Locate and identify every blood parasite.
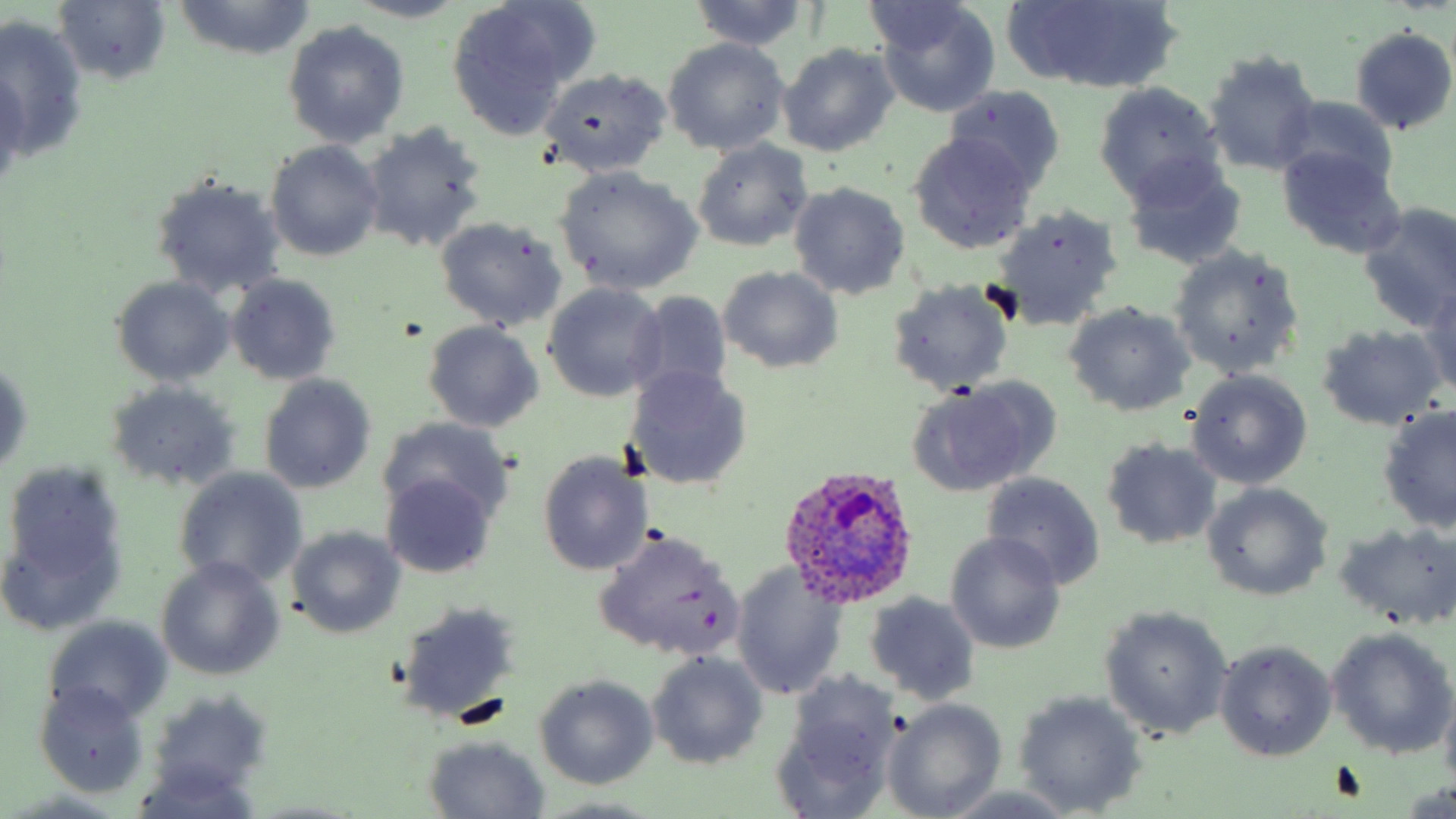
Approximate bounding boxes as named x1/y1/x2/y2 corners in pixels.
Plasmodium ovale-infected red blood cells: (x1=779, y1=466, x2=920, y2=608).
No Plasmodium falciparum, Plasmodium malariae, Plasmodium vivax, Babesia divergens, or Trypanosoma brucei observed.

Summary:
  - Uninfected red blood cell locations: (x1=54, y1=0, x2=173, y2=88), (x1=349, y1=0, x2=469, y2=24), (x1=170, y1=1, x2=321, y2=62), (x1=688, y1=1, x2=811, y2=52), (x1=1015, y1=1, x2=1177, y2=92), (x1=859, y1=3, x2=982, y2=59), (x1=872, y1=3, x2=1001, y2=117), (x1=443, y1=5, x2=585, y2=137), (x1=0, y1=17, x2=87, y2=158), (x1=283, y1=20, x2=410, y2=147), (x1=1348, y1=25, x2=1455, y2=135), (x1=662, y1=38, x2=791, y2=155), (x1=778, y1=43, x2=899, y2=156), (x1=1202, y1=49, x2=1322, y2=175), (x1=539, y1=67, x2=672, y2=176), (x1=0, y1=71, x2=27, y2=190), (x1=1093, y1=80, x2=1225, y2=205), (x1=945, y1=85, x2=1064, y2=195), (x1=1278, y1=95, x2=1402, y2=199), (x1=359, y1=122, x2=489, y2=255), (x1=908, y1=134, x2=1037, y2=256), (x1=691, y1=139, x2=814, y2=252), (x1=266, y1=140, x2=384, y2=261), (x1=1277, y1=146, x2=1407, y2=259), (x1=1119, y1=156, x2=1248, y2=271), (x1=554, y1=166, x2=703, y2=295), (x1=150, y1=174, x2=287, y2=299), (x1=788, y1=182, x2=912, y2=300), (x1=1356, y1=201, x2=1456, y2=329), (x1=988, y1=204, x2=1124, y2=330), (x1=435, y1=216, x2=567, y2=331), (x1=1168, y1=245, x2=1303, y2=378), (x1=718, y1=266, x2=844, y2=374), (x1=225, y1=274, x2=342, y2=386), (x1=110, y1=276, x2=236, y2=387), (x1=885, y1=279, x2=1015, y2=395), (x1=542, y1=283, x2=668, y2=402), (x1=1419, y1=288, x2=1456, y2=397), (x1=624, y1=291, x2=735, y2=405), (x1=1063, y1=303, x2=1195, y2=418), (x1=422, y1=321, x2=544, y2=434), (x1=1316, y1=323, x2=1448, y2=433), (x1=1, y1=355, x2=33, y2=482), (x1=626, y1=365, x2=753, y2=490), (x1=1186, y1=369, x2=1313, y2=489), (x1=258, y1=374, x2=377, y2=494), (x1=905, y1=379, x2=1056, y2=497), (x1=104, y1=380, x2=240, y2=492), (x1=1377, y1=407, x2=1456, y2=535), (x1=376, y1=415, x2=512, y2=527), (x1=1100, y1=437, x2=1222, y2=550), (x1=536, y1=449, x2=654, y2=577), (x1=174, y1=467, x2=309, y2=590), (x1=3, y1=469, x2=129, y2=635), (x1=980, y1=471, x2=1106, y2=589), (x1=384, y1=474, x2=495, y2=578), (x1=1202, y1=484, x2=1333, y2=602), (x1=1335, y1=522, x2=1456, y2=629), (x1=591, y1=526, x2=744, y2=662), (x1=287, y1=527, x2=408, y2=640), (x1=944, y1=532, x2=1067, y2=655), (x1=157, y1=557, x2=284, y2=679), (x1=731, y1=563, x2=849, y2=701), (x1=863, y1=591, x2=982, y2=705), (x1=395, y1=600, x2=522, y2=728), (x1=1099, y1=605, x2=1233, y2=741), (x1=44, y1=617, x2=173, y2=725), (x1=1326, y1=628, x2=1454, y2=760), (x1=1213, y1=640, x2=1337, y2=762), (x1=645, y1=654, x2=769, y2=769), (x1=533, y1=674, x2=659, y2=789), (x1=772, y1=674, x2=901, y2=818), (x1=33, y1=681, x2=151, y2=798), (x1=145, y1=690, x2=268, y2=796), (x1=1013, y1=690, x2=1148, y2=815), (x1=883, y1=698, x2=1006, y2=818), (x1=423, y1=736, x2=550, y2=817), (x1=129, y1=765, x2=267, y2=818), (x1=936, y1=784, x2=1089, y2=818)
  - Slide-level diagnosis: Plasmodium ovale
  - Field of view: single
  - Stain: May-Grünwald-Giemsa
  - Image size: 1456×819 pixels
  - Preparation: thin blood smear
  - Magnification: 1000x
  - Modality: light microscopy